Describe the morphology of the red blood cells.
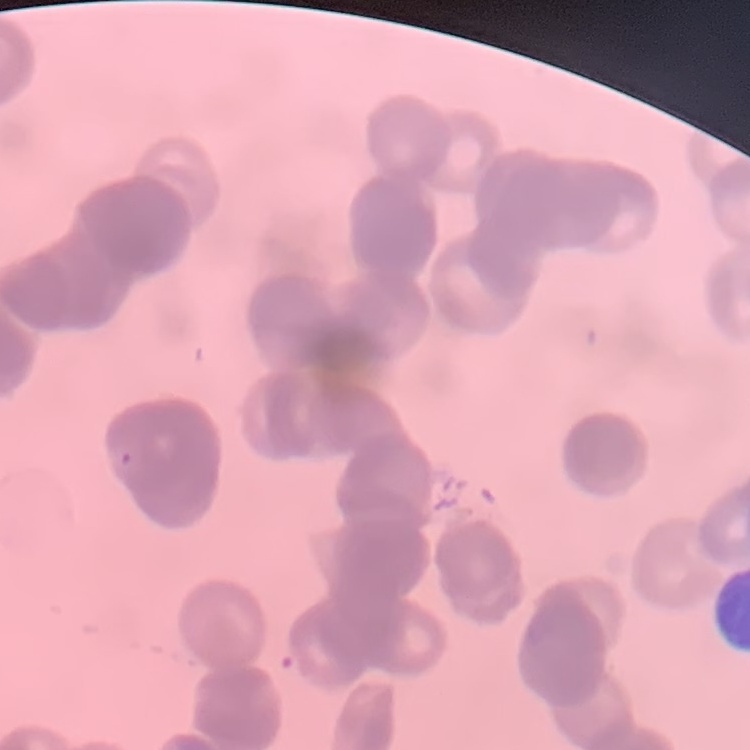
Rouleaux formation.

preparation: thin peripheral smear
stain: Field's or Giemsa
image_type: one tile cut from a larger photomicrograph